Report the malaria status of this cell.
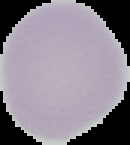

Uninfected.

image type = cell region segmented out of the field of view; surrounding area masked to black
preparation = thin blood film
image size = 130×145 pixels